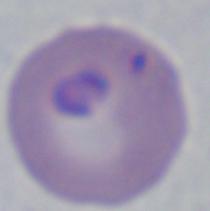
Summary:
  - Identification: Babesia
  - Modality: photomicrograph
  - Magnification: 1000x